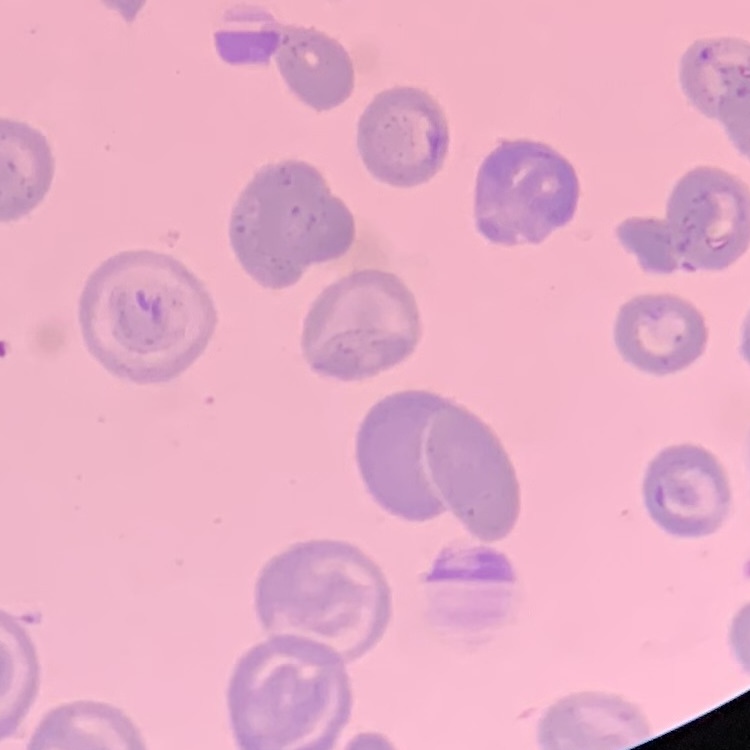
Summary:
  - Erythrocyte morphology: no rouleaux formation
  - Image type: square crop of a larger photomicrograph
  - Stain: Field's or Giemsa
  - Preparation: thin peripheral smear